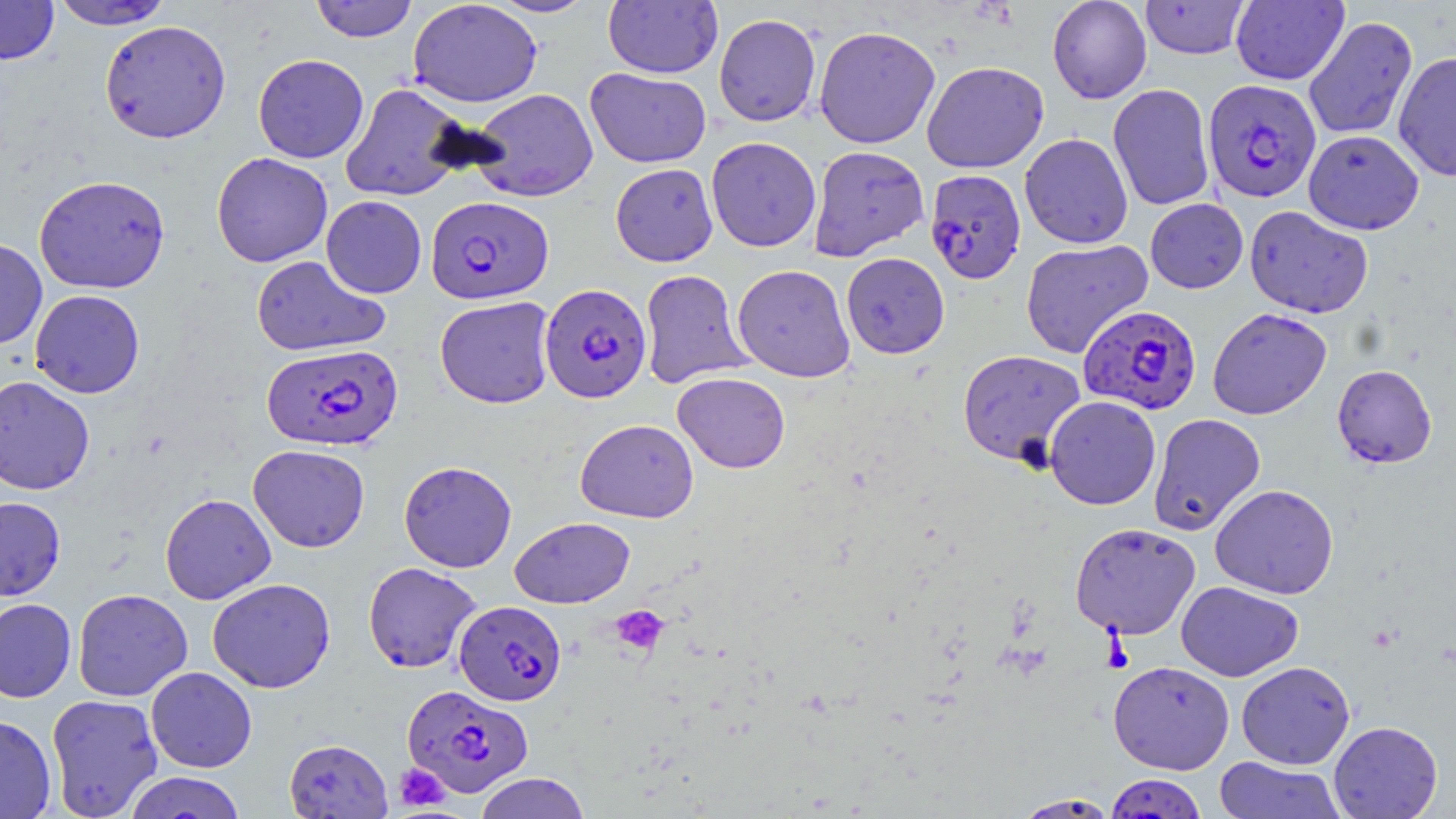

Summary:
  - Coordinate format: approximate bounding boxes as named x1/y1/x2/y2 corners in pixels
  - Platelet locations: (x1=609, y1=605, x2=669, y2=655), (x1=393, y1=763, x2=450, y2=811)
  - Plasmodium falciparum-infected red blood cell locations: (x1=1202, y1=78, x2=1321, y2=203), (x1=925, y1=169, x2=1027, y2=285), (x1=425, y1=195, x2=553, y2=305), (x1=539, y1=282, x2=652, y2=403), (x1=1078, y1=304, x2=1202, y2=415), (x1=262, y1=343, x2=403, y2=451), (x1=454, y1=600, x2=566, y2=705), (x1=402, y1=684, x2=533, y2=798), (x1=1105, y1=773, x2=1208, y2=818)
  - Uninfected red blood cell locations: (x1=310, y1=0, x2=418, y2=42), (x1=407, y1=0, x2=543, y2=108), (x1=489, y1=0, x2=597, y2=17), (x1=1046, y1=0, x2=1152, y2=104), (x1=1140, y1=0, x2=1251, y2=60), (x1=1230, y1=0, x2=1348, y2=85), (x1=0, y1=1, x2=59, y2=65), (x1=48, y1=1, x2=175, y2=30), (x1=603, y1=1, x2=722, y2=79), (x1=713, y1=13, x2=821, y2=127), (x1=1303, y1=15, x2=1418, y2=140), (x1=99, y1=19, x2=232, y2=143), (x1=814, y1=25, x2=940, y2=149), (x1=1393, y1=51, x2=1456, y2=181), (x1=253, y1=53, x2=369, y2=163), (x1=922, y1=60, x2=1049, y2=173), (x1=584, y1=67, x2=712, y2=168), (x1=340, y1=83, x2=470, y2=202), (x1=1108, y1=83, x2=1215, y2=211), (x1=469, y1=88, x2=598, y2=202), (x1=1303, y1=129, x2=1424, y2=234), (x1=1019, y1=132, x2=1133, y2=249), (x1=705, y1=136, x2=821, y2=252), (x1=808, y1=145, x2=929, y2=261), (x1=211, y1=152, x2=333, y2=267), (x1=610, y1=163, x2=718, y2=267), (x1=33, y1=174, x2=170, y2=294), (x1=321, y1=195, x2=427, y2=298), (x1=1145, y1=198, x2=1248, y2=294), (x1=1244, y1=205, x2=1373, y2=318), (x1=0, y1=237, x2=48, y2=350), (x1=1020, y1=239, x2=1153, y2=359), (x1=841, y1=252, x2=950, y2=358), (x1=251, y1=255, x2=390, y2=357), (x1=732, y1=264, x2=855, y2=382), (x1=638, y1=269, x2=753, y2=390), (x1=30, y1=289, x2=145, y2=398), (x1=435, y1=295, x2=556, y2=409), (x1=1207, y1=307, x2=1332, y2=420), (x1=957, y1=349, x2=1086, y2=467), (x1=1332, y1=364, x2=1437, y2=468), (x1=672, y1=371, x2=791, y2=473), (x1=0, y1=376, x2=95, y2=495), (x1=1045, y1=395, x2=1161, y2=510), (x1=1148, y1=413, x2=1266, y2=536), (x1=575, y1=418, x2=699, y2=523), (x1=248, y1=444, x2=370, y2=552), (x1=398, y1=460, x2=517, y2=572), (x1=1209, y1=484, x2=1339, y2=599), (x1=159, y1=493, x2=276, y2=604), (x1=0, y1=496, x2=66, y2=601), (x1=510, y1=516, x2=635, y2=608), (x1=1069, y1=522, x2=1201, y2=640), (x1=362, y1=561, x2=482, y2=673), (x1=207, y1=577, x2=335, y2=693), (x1=1176, y1=581, x2=1304, y2=682), (x1=72, y1=588, x2=193, y2=701), (x1=0, y1=598, x2=77, y2=702), (x1=1108, y1=660, x2=1235, y2=775), (x1=1236, y1=661, x2=1355, y2=769), (x1=146, y1=666, x2=257, y2=772), (x1=45, y1=694, x2=163, y2=818), (x1=0, y1=715, x2=56, y2=819), (x1=1329, y1=721, x2=1443, y2=819), (x1=283, y1=738, x2=393, y2=818), (x1=1214, y1=756, x2=1346, y2=818), (x1=125, y1=771, x2=247, y2=818), (x1=474, y1=772, x2=591, y2=819), (x1=1011, y1=793, x2=1121, y2=818)
  - Slide-level diagnosis: Plasmodium falciparum
  - Field of view: single
  - Preparation: thin blood smear
  - Modality: optical microscopy
  - Image size: 1456×819 pixels
  - Magnification: 1000x
  - Stain: May-Grünwald-Giemsa